Report the malaria status of this cell.
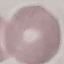
Uninfected.

Cell patch, automatically extracted from a larger field of view and resized to 64 × 64 pixels. Thin smear of blood. Photographed with a smartphone camera at the microscope eyepiece. Giemsa stain.